Describe the morphology of the red blood cells.
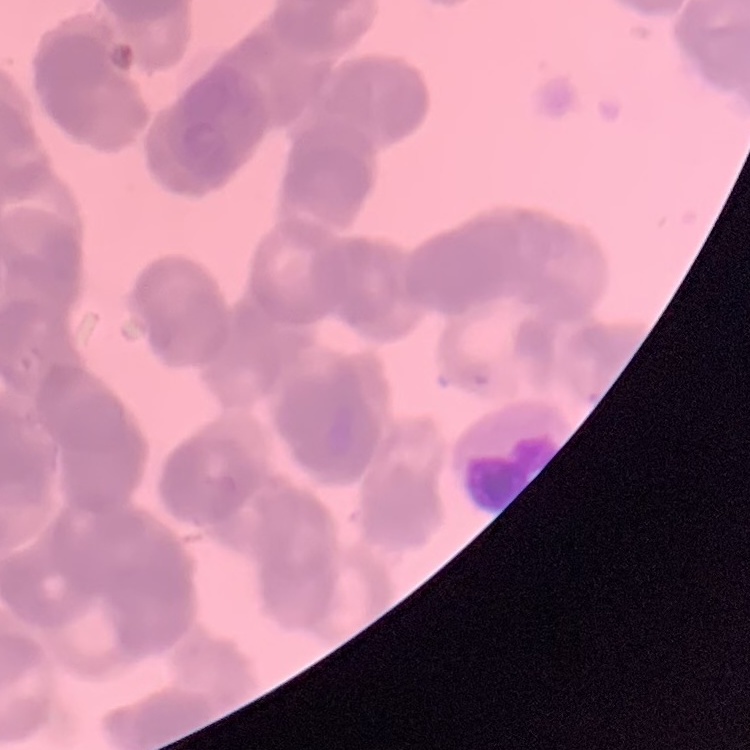
They show rouleaux formation.

preparation = thin peripheral smear
image type = one tile cut from a larger photomicrograph
stain = Field's or Giemsa